Locate every Plasmodium parasite.
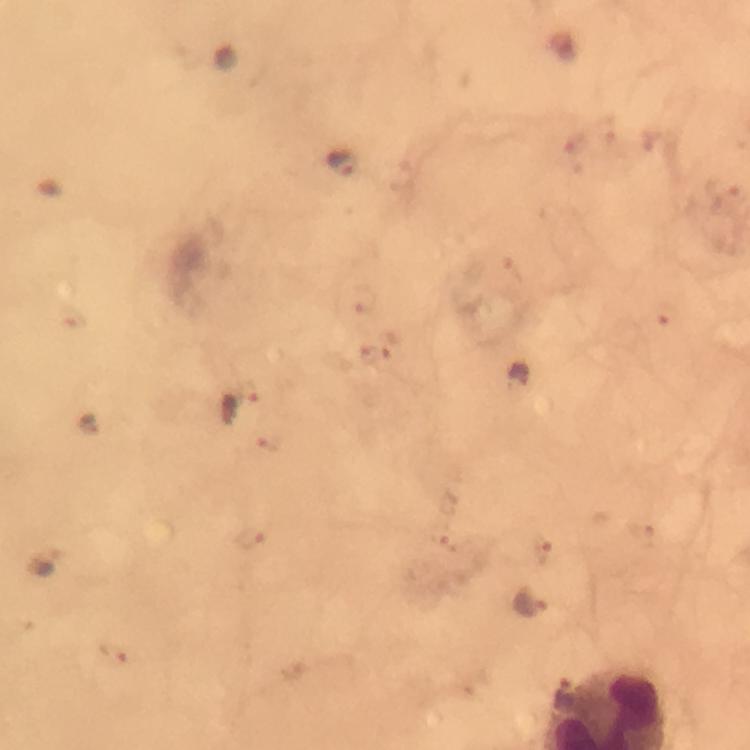
Approximate centers as {x, y} in pixels.
Plasmodium parasites: {344, 162}, {240, 403}, {530, 603}, {565, 697}.

Immersion oil was used. Image is 750×750 pixels. At 100x magnification. Thick blood smear. Giemsa-stained preparation. A crop from one field of view. From a malaria diagnostic workup. Smartphone photograph taken through a microscope.